Outline each blood parasite and name the species.
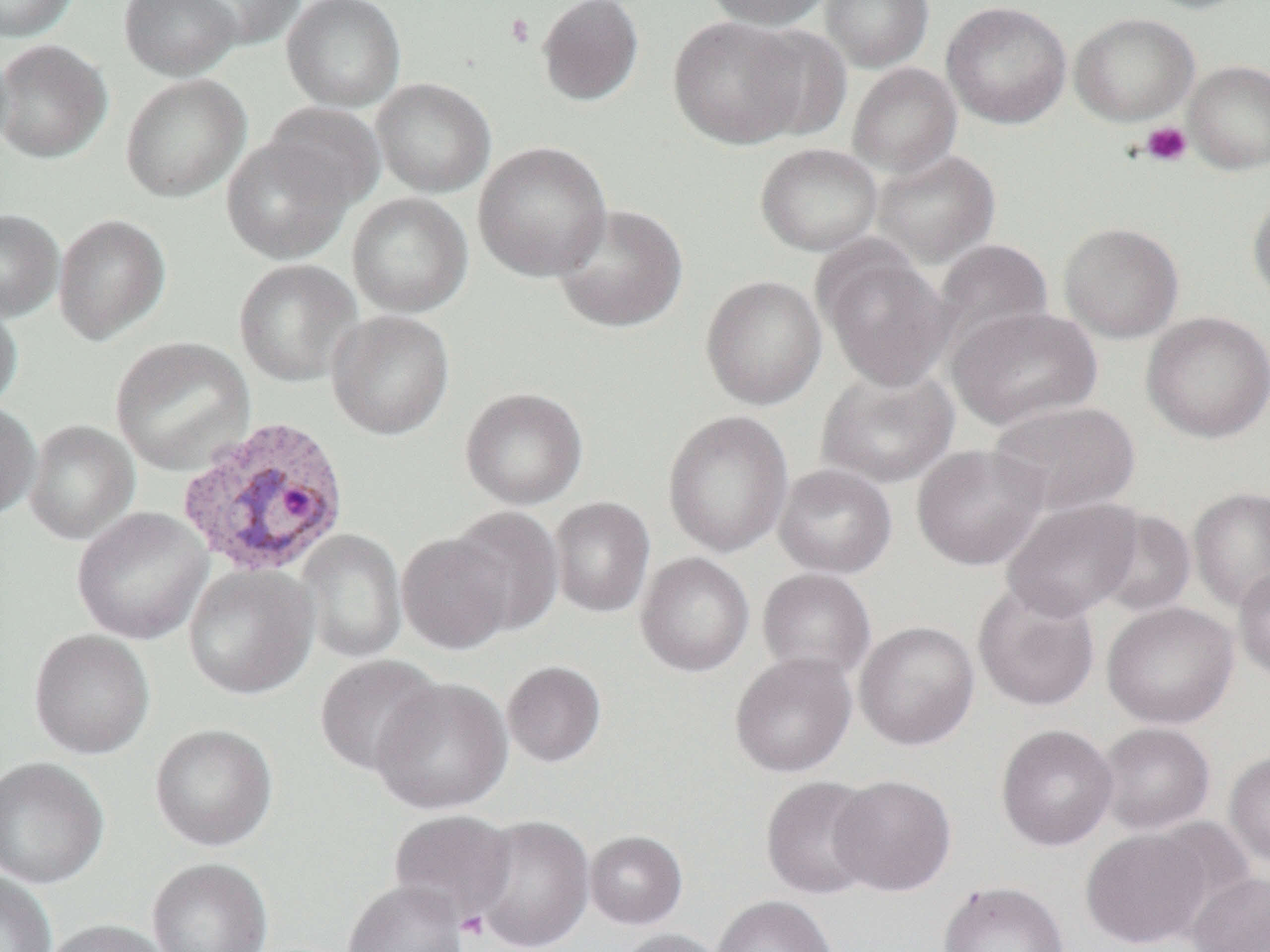

Approximate bounding boxes as (x1,y1)-(x2,y2) corner pairs in pixels.
Plasmodium vivax-infected red blood cells: (178,419)-(352,581).
No Plasmodium falciparum, Plasmodium ovale, Plasmodium malariae, Babesia divergens, or Trypanosoma brucei observed.

Platelet locations: (505,13)-(535,47), (1140,121)-(1192,167), (457,911)-(490,942). Uninfected red blood cell locations: (0,0)-(78,42), (119,0)-(242,80), (180,0)-(305,50), (282,0)-(406,112), (536,0)-(645,106), (700,0)-(834,30), (819,0)-(934,72), (1137,0)-(1256,15), (941,1)-(1072,129), (1069,12)-(1200,126), (667,15)-(812,149), (742,24)-(856,141), (0,39)-(112,164), (1183,59)-(1270,175), (847,63)-(962,178), (120,73)-(251,203), (371,78)-(495,198), (261,103)-(385,212), (221,135)-(354,265), (473,141)-(612,282), (755,142)-(883,256), (871,149)-(1001,267), (1248,190)-(1270,307), (346,192)-(474,317), (552,203)-(688,333), (0,208)-(64,322), (53,213)-(171,346), (1058,222)-(1184,343), (932,239)-(1054,356), (817,243)-(953,392), (234,259)-(362,387), (700,275)-(827,410), (0,298)-(23,415), (947,306)-(1102,430), (327,310)-(455,440), (1141,311)-(1270,443), (110,336)-(255,474), (816,366)-(959,489), (460,387)-(588,509), (988,400)-(1141,515), (0,401)-(41,520), (662,409)-(793,558), (23,419)-(140,545), (911,444)-(1050,571), (773,464)-(897,579), (1188,487)-(1270,612), (550,497)-(655,618), (1001,498)-(1144,621), (444,506)-(565,637), (72,507)-(212,644), (1091,508)-(1197,617), (296,530)-(407,664), (396,532)-(515,655), (635,552)-(755,677), (183,563)-(318,700), (1233,564)-(1270,684), (757,568)-(877,684), (972,581)-(1100,713), (1102,601)-(1238,729), (855,620)-(979,750), (28,629)-(155,760), (730,652)-(856,777), (314,654)-(444,777), (502,660)-(606,767), (371,677)-(512,816), (1096,722)-(1216,835), (149,723)-(278,852), (996,724)-(1118,851), (1224,750)-(1270,867), (0,756)-(110,890), (829,774)-(956,896), (761,776)-(883,901), (387,809)-(517,924), (471,815)-(595,952), (1081,829)-(1212,948), (585,831)-(687,929), (146,857)-(273,952), (1187,871)-(1270,952), (0,872)-(58,952), (343,881)-(469,952), (939,881)-(1069,952), (711,895)-(837,952), (42,918)-(174,952), (615,928)-(726,952). Slide-level diagnosis: Plasmodium vivax. 1000x magnification. Optical microscopy. Image is 1270×952 pixels. Thin blood smear. One field of a larger specimen.